Outline each blood parasite and name the species.
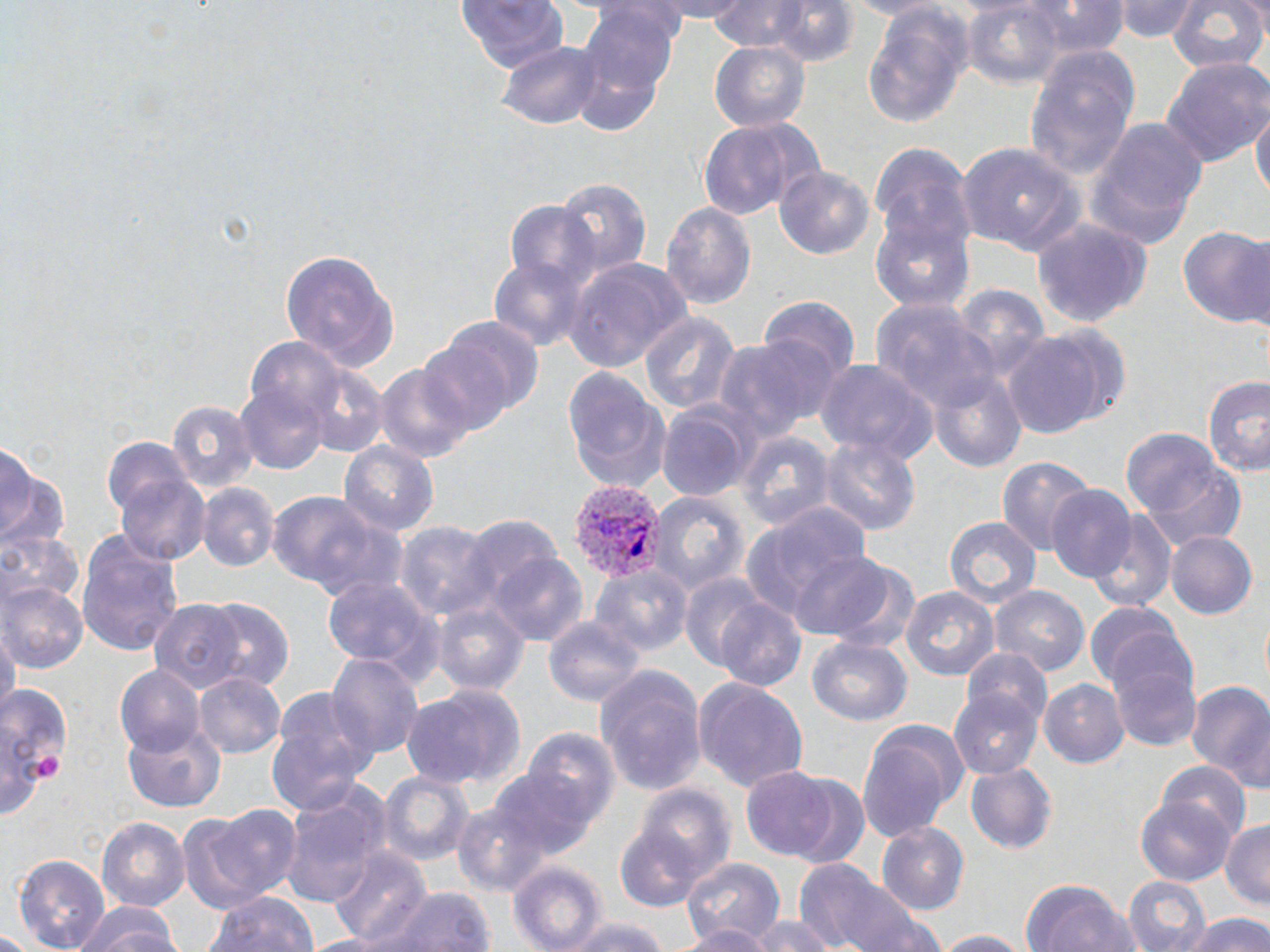
Approximate bounding boxes as (x1, y1, x2, y2) in pixels.
Plasmodium vivax-infected red blood cells: (567, 478, 665, 584).
No Plasmodium falciparum, Plasmodium ovale, Plasmodium malariae, Babesia divergens, or Trypanosoma brucei observed.

Platelet locations: (31, 753, 64, 784). Uninfected red blood cell locations: (643, 0, 752, 20), (710, 0, 822, 53), (840, 0, 946, 20), (1118, 0, 1196, 43), (458, 1, 567, 78), (766, 1, 860, 68), (963, 1, 1069, 90), (1016, 1, 1132, 56), (1167, 2, 1267, 76), (578, 6, 679, 108), (862, 7, 972, 131), (498, 38, 603, 130), (708, 41, 809, 130), (1025, 46, 1139, 182), (1161, 58, 1270, 168), (1252, 104, 1269, 208), (696, 116, 821, 222), (1085, 120, 1207, 249), (867, 140, 976, 269), (958, 144, 1085, 259), (774, 162, 877, 258), (551, 174, 652, 278), (502, 200, 601, 301), (660, 200, 757, 311), (869, 212, 975, 315), (1031, 216, 1151, 331), (1178, 224, 1270, 329), (282, 248, 399, 370), (563, 256, 695, 373), (488, 258, 587, 351), (757, 298, 859, 390), (869, 298, 993, 414), (637, 310, 740, 419), (419, 322, 539, 432), (1000, 329, 1123, 436), (708, 335, 836, 441), (299, 358, 389, 459), (373, 358, 482, 465), (817, 358, 936, 465), (562, 367, 673, 492), (928, 370, 1029, 476), (235, 372, 330, 476), (1202, 374, 1270, 476), (166, 400, 256, 497), (656, 404, 754, 504), (1120, 430, 1248, 551), (737, 431, 832, 529), (821, 436, 920, 539), (102, 437, 200, 535), (339, 441, 438, 541), (0, 449, 64, 556), (996, 454, 1096, 556), (115, 466, 211, 567), (198, 484, 276, 571), (1045, 487, 1136, 583), (647, 489, 748, 595), (266, 490, 396, 600), (742, 501, 870, 619), (1089, 510, 1176, 614), (945, 517, 1041, 607), (396, 521, 497, 621), (0, 528, 81, 619), (73, 528, 185, 654), (1167, 531, 1258, 619), (485, 548, 591, 648), (787, 550, 900, 643), (594, 567, 693, 659), (322, 573, 444, 685), (679, 574, 774, 674), (3, 580, 86, 671), (899, 583, 1001, 682), (990, 585, 1088, 676), (714, 594, 808, 691), (432, 600, 530, 699), (150, 601, 246, 694), (202, 602, 295, 693), (1086, 603, 1185, 688), (544, 614, 644, 706), (2, 629, 16, 727), (1102, 629, 1204, 753), (808, 637, 912, 725), (961, 651, 1055, 735), (326, 655, 423, 764), (115, 664, 203, 753), (594, 669, 706, 796), (195, 674, 285, 757), (693, 676, 809, 793), (1040, 677, 1129, 769), (1186, 681, 1270, 790), (0, 685, 76, 787), (402, 685, 527, 792), (266, 686, 374, 814), (951, 691, 1042, 777), (857, 719, 968, 840), (509, 722, 617, 846), (123, 723, 227, 812), (0, 726, 45, 819), (1156, 762, 1250, 842), (966, 765, 1057, 854), (741, 768, 841, 860), (377, 771, 473, 868), (786, 776, 873, 870), (636, 786, 737, 886), (279, 793, 387, 905), (1136, 793, 1235, 884), (452, 795, 559, 895), (188, 804, 303, 914), (98, 816, 190, 914), (1220, 821, 1270, 909), (614, 822, 710, 913), (877, 824, 971, 916), (327, 846, 431, 944), (12, 854, 112, 951), (680, 855, 787, 945), (796, 861, 939, 952), (507, 862, 606, 951), (1121, 874, 1214, 952), (1019, 877, 1140, 952), (370, 885, 496, 952), (204, 893, 319, 952), (73, 901, 186, 952), (1188, 913, 1270, 952), (748, 916, 832, 952), (563, 917, 675, 952), (678, 923, 772, 952), (925, 929, 1036, 951). Slide-level diagnosis: Plasmodium vivax. May-Grünwald-Giemsa stain. One field of a larger specimen. Captured at 1000x magnification. Image is 1270×952 pixels. Light microscopy. Thin blood smear.